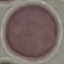

{
  "malaria_status": "uninfected",
  "preparation": "thin smear",
  "image_type": "cell patch, automatically extracted from a larger field of view and resized to 64 × 64 pixels",
  "stain": "Giemsa",
  "capture": "smartphone through the microscope eyepiece"
}